Identify the blood parasite species.
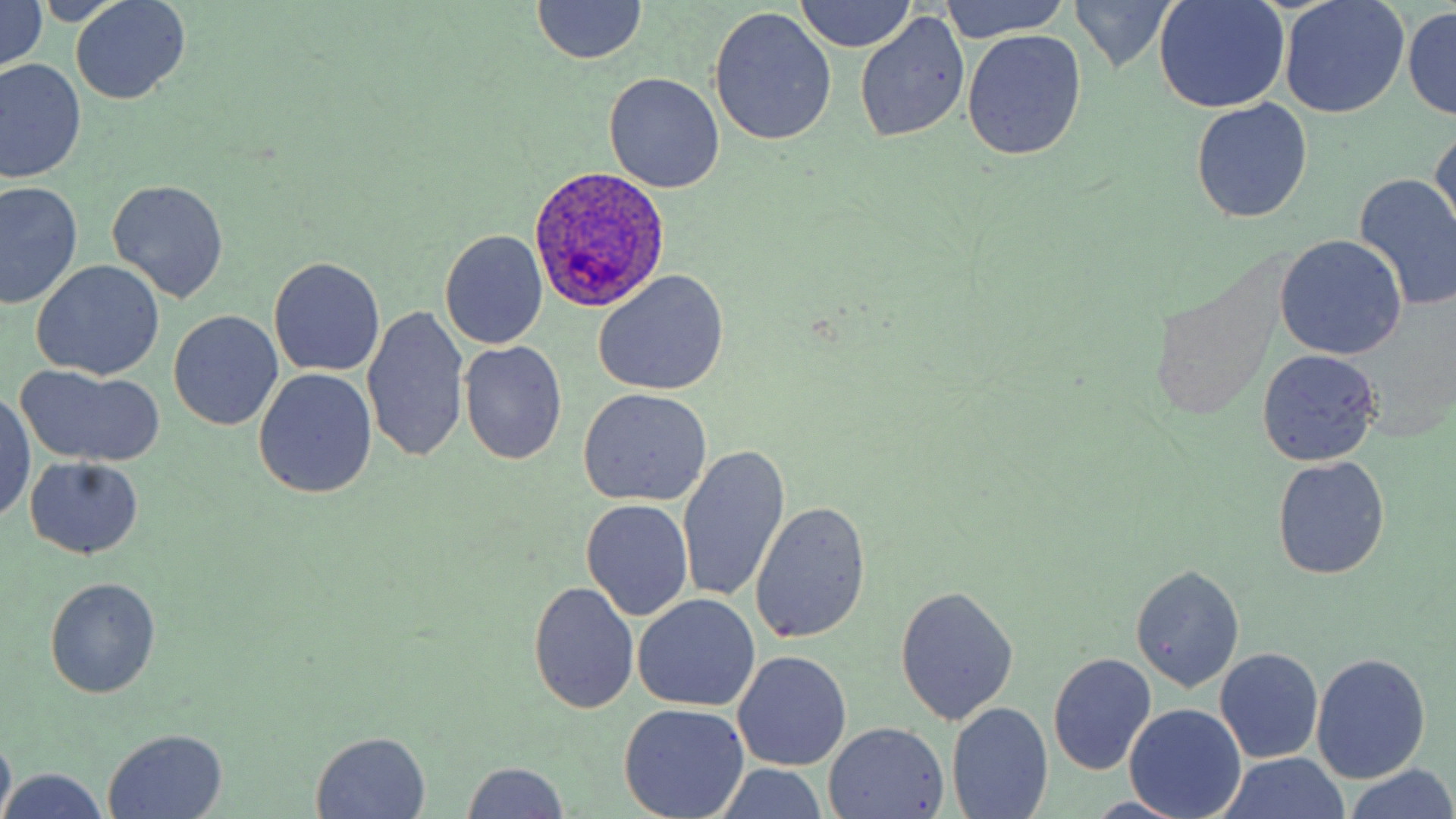
Plasmodium ovale.

Approximate bounding boxes as [x1, y1, x2, y2] in pixels. Uninfected red blood cell locations: [0, 0, 48, 78], [940, 0, 1071, 44], [1068, 0, 1182, 72], [1156, 0, 1290, 114], [1279, 0, 1408, 119], [71, 1, 190, 105], [532, 1, 647, 65], [796, 1, 915, 54], [709, 7, 837, 146], [1404, 8, 1456, 119], [855, 13, 969, 143], [963, 30, 1086, 160], [1, 58, 85, 183], [604, 72, 726, 192], [1192, 99, 1312, 222], [1429, 125, 1456, 240], [1355, 173, 1456, 305], [108, 178, 229, 304], [1, 180, 82, 310], [1311, 205, 1456, 338], [440, 230, 548, 350], [1274, 235, 1407, 361], [270, 257, 385, 378], [32, 260, 165, 381], [593, 270, 730, 396], [362, 305, 470, 462], [168, 309, 283, 432], [459, 340, 567, 466], [1256, 350, 1381, 466], [15, 368, 163, 468], [253, 368, 377, 499], [578, 390, 712, 507], [1, 392, 36, 523], [677, 445, 790, 606], [23, 456, 144, 560], [1272, 457, 1390, 580], [581, 498, 694, 621], [752, 500, 872, 645], [1131, 563, 1244, 692], [44, 577, 160, 698], [529, 579, 640, 714], [894, 585, 1018, 727], [633, 594, 760, 713], [1215, 648, 1324, 763], [733, 650, 851, 771], [1047, 653, 1157, 775], [1312, 654, 1430, 784], [619, 702, 749, 818], [949, 703, 1053, 819], [1126, 703, 1247, 819], [824, 722, 951, 817], [102, 729, 229, 818], [0, 730, 15, 819], [309, 731, 432, 819], [1217, 754, 1354, 819], [459, 762, 571, 818], [1343, 765, 1456, 819], [3, 768, 110, 819]. Plasmodium ovale-infected red blood cell locations: [529, 164, 671, 311]. Image is 1456×819 pixels. 1000x magnification. Light microscopy. May-Grünwald-Giemsa-stained preparation. Thin blood smear. Single field of view.